Locate every malaria parasite.
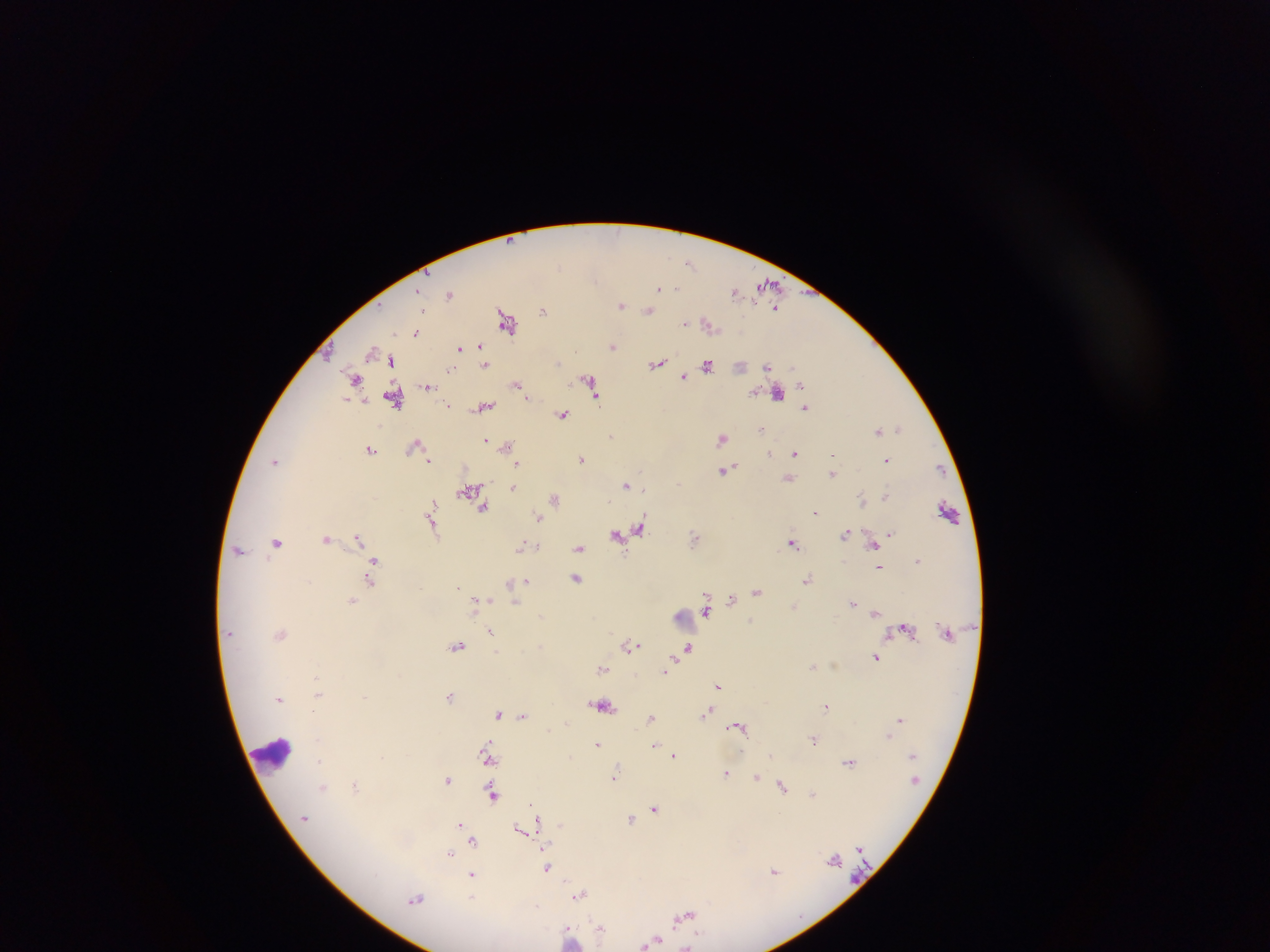
Approximate centers as [x, y] in pixels.
Malaria parasites: [689, 263], [596, 280], [769, 284], [659, 287], [676, 287], [734, 291], [449, 294], [621, 305], [776, 308], [422, 309], [544, 310], [649, 311], [506, 321], [685, 322], [709, 324], [417, 331], [612, 346], [481, 347], [459, 348], [372, 351], [329, 353], [386, 359], [392, 361], [657, 364], [707, 364], [485, 365], [767, 367], [452, 368], [683, 377], [354, 379], [589, 379], [801, 384], [428, 385], [518, 385], [591, 387], [777, 394], [595, 397], [394, 399], [349, 400], [448, 405], [483, 407], [805, 408], [563, 414], [899, 428], [761, 430], [879, 431], [611, 436], [721, 438], [486, 440], [415, 446], [506, 446], [371, 449], [795, 453], [769, 454], [428, 458], [581, 459], [886, 460], [276, 461], [518, 464], [939, 469], [725, 471], [833, 473], [789, 479], [627, 485], [513, 486], [470, 489], [643, 489], [886, 495], [554, 498], [862, 500], [609, 501], [484, 507], [432, 508], [948, 511], [816, 512], [431, 517], [539, 517], [432, 524], [640, 528], [623, 532], [890, 533], [845, 534], [616, 535], [695, 537], [358, 538], [326, 539], [277, 542], [873, 543], [792, 544], [522, 546], [580, 547], [239, 550], [918, 560], [374, 562], [880, 567], [576, 577], [808, 579], [371, 580], [526, 581], [511, 583], [757, 591], [732, 600], [351, 601], [477, 602], [515, 602], [853, 603], [794, 607], [706, 610], [876, 613], [541, 615], [751, 621], [905, 627], [491, 632], [281, 634], [540, 645], [631, 645], [458, 646], [688, 647], [875, 657], [813, 666], [602, 668], [666, 669], [317, 677], [718, 686], [318, 693], [365, 696], [449, 696], [279, 698], [602, 705], [826, 706], [707, 712], [499, 713], [523, 714], [650, 718], [900, 719], [739, 727], [889, 736], [814, 741], [597, 744], [655, 745], [912, 754], [771, 755], [488, 756], [675, 756], [319, 760], [849, 762], [726, 773], [615, 775], [756, 777], [447, 780], [324, 787], [356, 787], [783, 787], [813, 794], [492, 795], [531, 803], [654, 808], [535, 809], [304, 818], [537, 819], [630, 820], [460, 824], [519, 828], [474, 841], [450, 853], [834, 858], [547, 868], [775, 871], [472, 876], [579, 894], [416, 899], [683, 917], [601, 929], [569, 934], [652, 941], [688, 946].

Summary:
  - Leukocyte locations: [683, 620], [272, 754]
  - Capture: mobile-phone photograph through a microscope
  - Preparation: thick blood film
  - Field of view: single
  - Image size: 1270×952 pixels
  - Country: Ghana